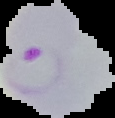
preparation = thin blood film
result = Plasmodium parasites identified
image size = 115×118 pixels
image type = segmented cell region on a black background